Describe the morphology of the erythrocytes.
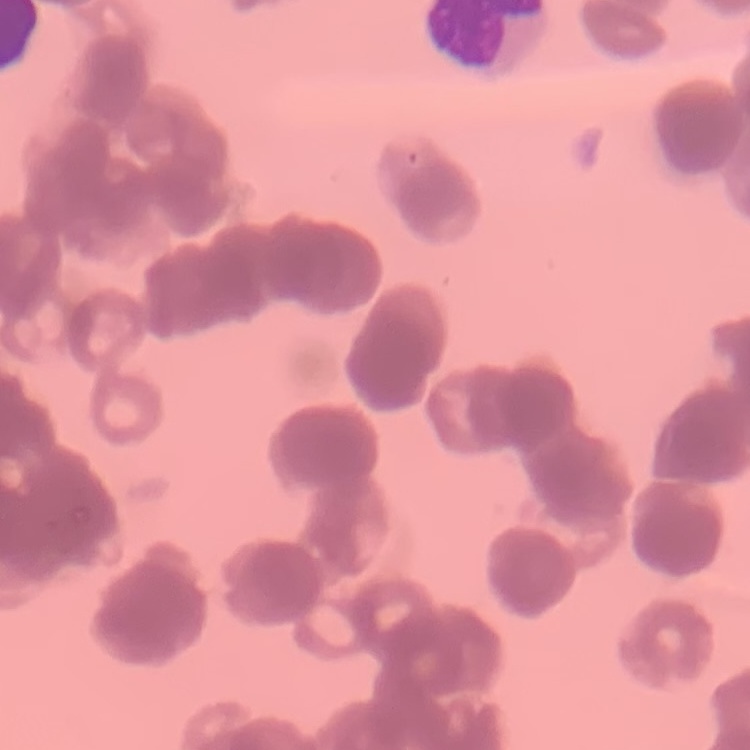
Rouleaux formation.

Summary:
  - Image type: square crop of a larger photomicrograph
  - Preparation: thin blood film
  - Stain: Field's or Giemsa